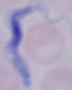
Captured at 1000x magnification. Micrograph. A trypanosome is shown.